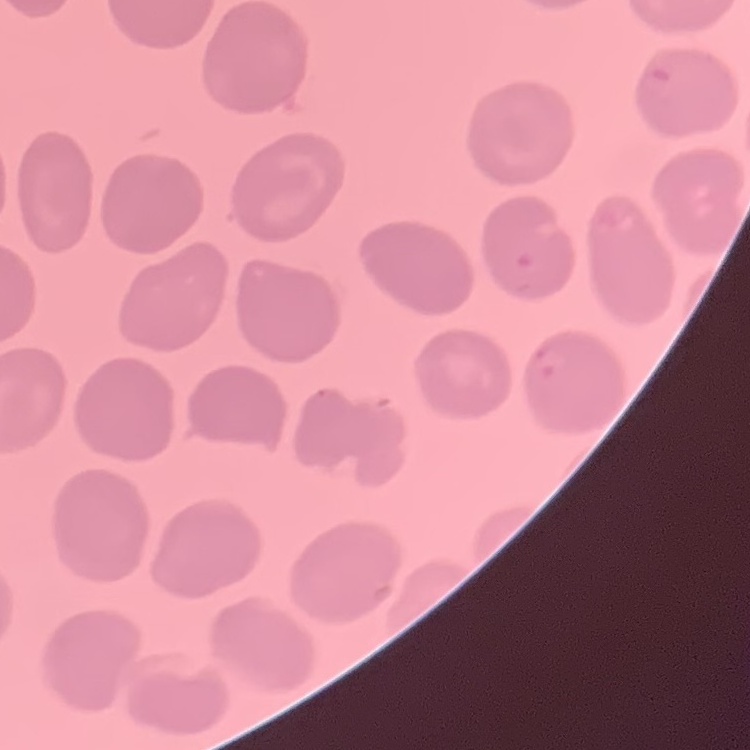
The red blood cells show no rouleaux formation. One tile cut from a larger photomicrograph. Thin blood smear. Field's or Giemsa stain.